Point out each leukocyte.
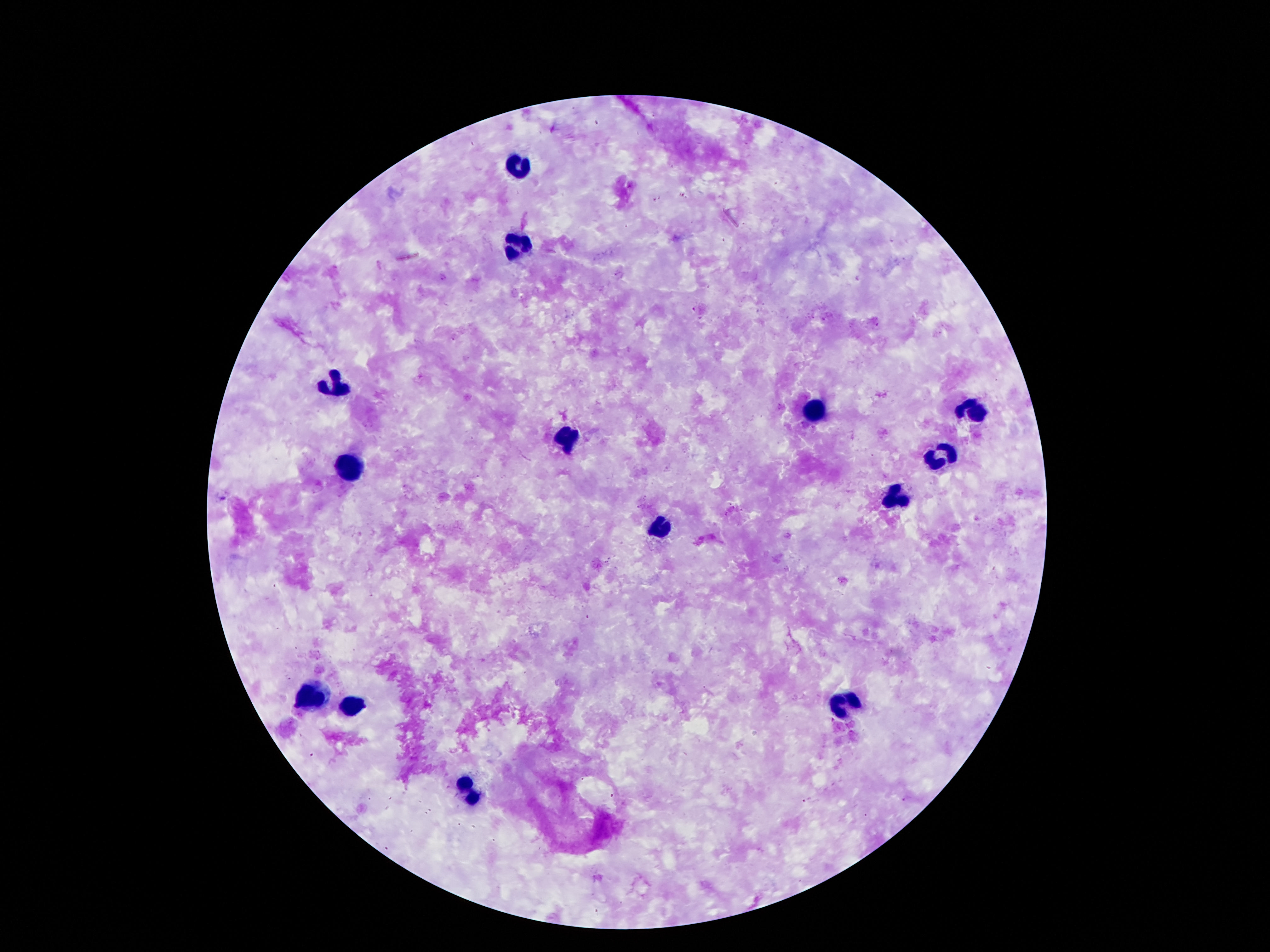
Approximate centers as [x, y] in pixels.
Leukocytes: [521, 164], [514, 246], [336, 383], [972, 405], [813, 408], [563, 439], [936, 460], [351, 464], [895, 497], [659, 527], [311, 697], [846, 703], [353, 707], [470, 793].

Thick peripheral-blood smear. Giemsa-stained preparation. Photographed through the microscope eyepiece with a smartphone camera. 100x magnification. Single field of view. Patient malaria status: uninfected. Image is 1270×952 pixels.